Report the malaria status of this cell.
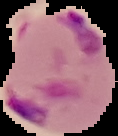

Parasitized.

image_type: cell region segmented out of the field of view; surrounding area masked to black
preparation: thin blood smear
image_size: 118×136 pixels